Describe the morphology of the erythrocytes.
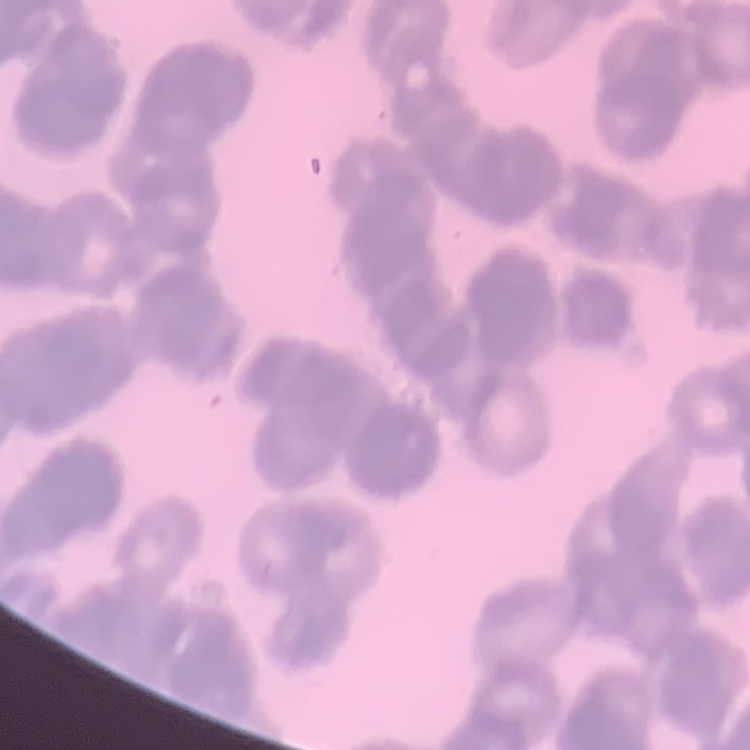
Rouleaux formation.

Summary:
  - Image type: square crop of a larger photomicrograph
  - Stain: Field's or Giemsa
  - Preparation: thin blood smear